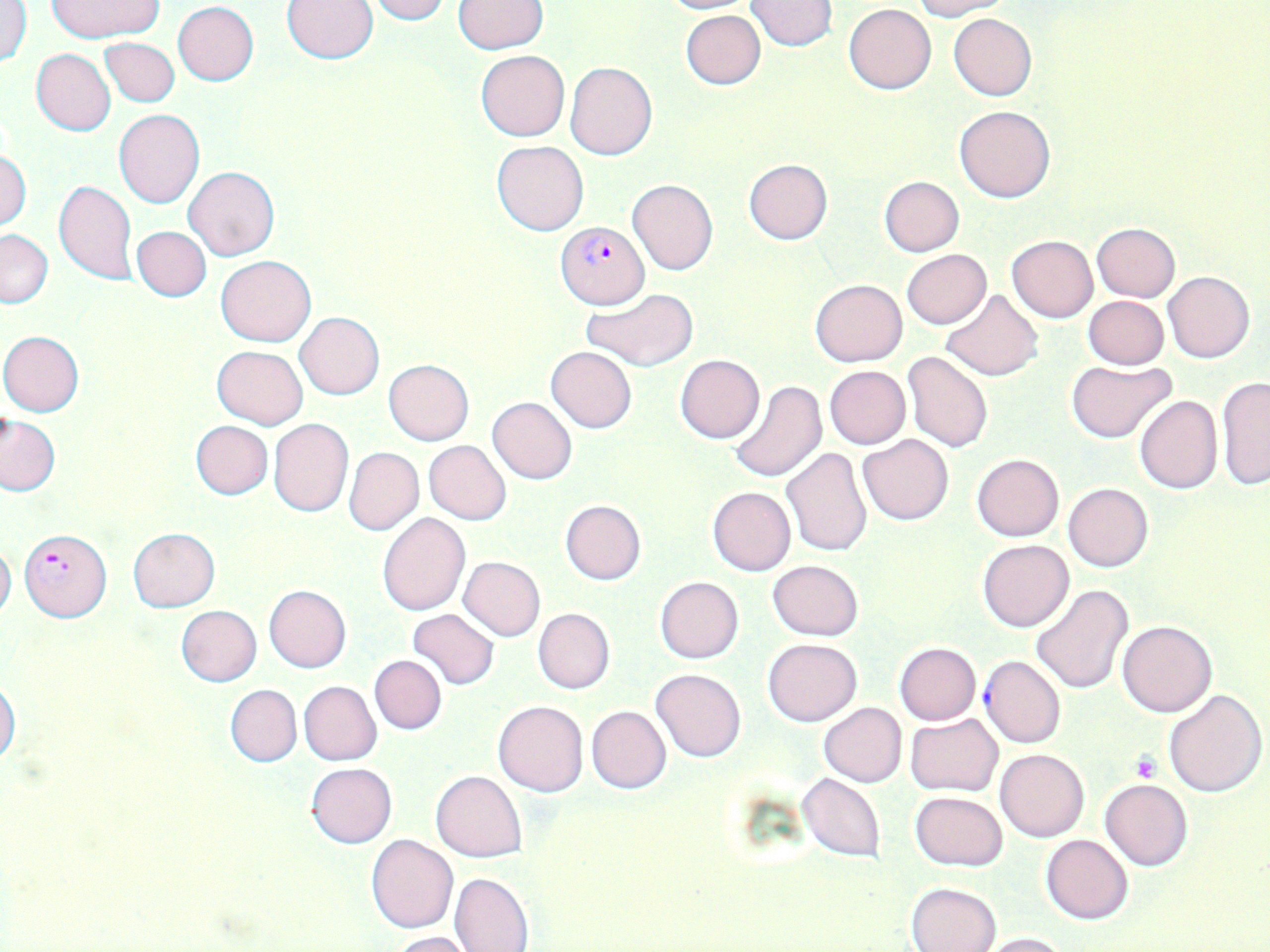
Summary:
  - Coordinate format: approximate bounding boxes as (x1, y1, x2, y2) in pixels
  - Platelet locations: (1131, 753, 1160, 780)
  - Plasmodium falciparum-infected red blood cell locations: (555, 220, 650, 309), (20, 527, 111, 623)
  - Uninfected red blood cell locations: (47, 0, 163, 41), (282, 0, 380, 64), (365, 0, 451, 23), (654, 0, 758, 15), (744, 0, 836, 51), (912, 0, 1011, 20), (452, 1, 548, 52), (1, 2, 31, 67), (172, 2, 260, 86), (844, 3, 936, 94), (681, 10, 765, 90), (948, 12, 1036, 101), (98, 38, 180, 108), (31, 49, 115, 136), (476, 50, 569, 140), (565, 61, 656, 160), (954, 105, 1056, 203), (112, 109, 205, 208), (492, 141, 588, 235), (0, 149, 31, 232), (743, 159, 832, 245), (185, 165, 278, 260), (879, 176, 965, 257), (628, 178, 718, 275), (53, 179, 138, 285), (1091, 223, 1180, 303), (131, 225, 211, 302), (0, 229, 53, 307), (1006, 235, 1097, 323), (901, 249, 993, 329), (216, 255, 316, 346), (1164, 271, 1255, 362), (810, 278, 907, 367), (584, 288, 701, 371), (940, 289, 1044, 381), (1083, 295, 1169, 370), (294, 311, 383, 400), (1, 331, 84, 416), (212, 345, 307, 428), (546, 346, 637, 432), (902, 350, 994, 453), (675, 354, 764, 443), (384, 359, 474, 445), (1067, 360, 1175, 443), (824, 366, 910, 448), (1216, 374, 1270, 492), (729, 381, 827, 483), (1134, 395, 1223, 495), (487, 397, 578, 484), (1, 415, 60, 495), (268, 419, 353, 517), (191, 420, 273, 500), (857, 433, 954, 525), (424, 440, 511, 525), (782, 446, 874, 558), (345, 447, 423, 534), (972, 454, 1064, 541), (1063, 483, 1153, 572), (707, 487, 795, 575), (560, 499, 646, 585), (377, 513, 469, 615), (128, 528, 220, 611), (977, 539, 1074, 631), (0, 541, 16, 622), (459, 557, 545, 641), (767, 560, 862, 639), (655, 576, 743, 662), (1031, 584, 1133, 695), (263, 585, 351, 673), (175, 606, 262, 687), (407, 608, 500, 690), (533, 608, 614, 694), (1118, 620, 1217, 717), (762, 638, 861, 726), (894, 642, 981, 724), (369, 655, 446, 734), (980, 655, 1066, 749), (650, 668, 746, 762), (0, 681, 20, 766), (298, 681, 382, 765), (225, 685, 302, 767), (1163, 689, 1266, 795), (493, 700, 588, 796), (819, 702, 907, 787), (586, 706, 672, 793), (905, 714, 1002, 796), (995, 748, 1090, 842), (306, 763, 397, 848), (431, 771, 527, 862), (796, 773, 887, 862), (1100, 777, 1193, 871), (909, 790, 1008, 871), (366, 834, 457, 933), (1041, 834, 1133, 924), (450, 872, 534, 952), (907, 881, 1002, 952), (388, 931, 477, 952), (978, 931, 1068, 951)
  - Slide-level diagnosis: Plasmodium falciparum
  - Preparation: thin blood film
  - Stain: May-Grünwald-Giemsa
  - Field of view: one of a larger specimen
  - Modality: optical microscopy
  - Image size: 1270×952 pixels
  - Magnification: 1000x